Name the parasite shown.
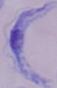

A trypanosome.

Summary:
  - Magnification: 1000x
  - Modality: micrograph